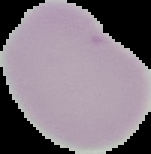 Segmented cell region on a black background. Result: negative for Plasmodium parasites. Image is 151×154 pixels. From a thin blood smear.